Report the malaria status of this cell.
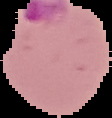
It is parasitized.

Image is 112×118 pixels. From a thin blood film. Cell region segmented out of the field of view; the surrounding area is masked to black.